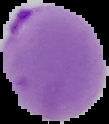
From a thin blood smear. Result: malaria parasites detected. Image is 109×124 pixels. Cell region segmented out of the field of view; the surrounding area is masked to black.